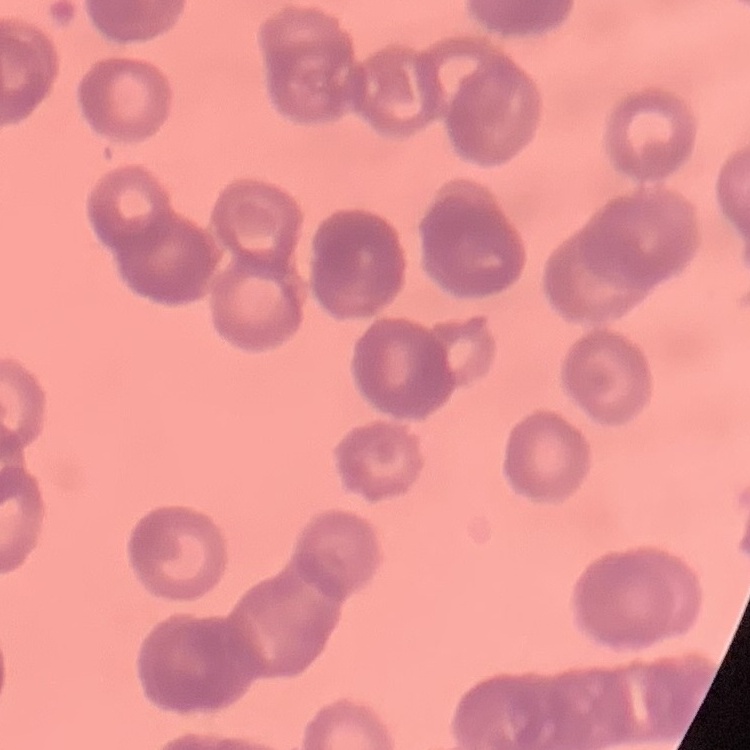
The red blood cells show rouleaux formation. Stained with either Field's or Giemsa. Square crop of a larger photomicrograph. Thin blood film.